Assess this cell for malaria.
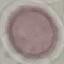

Uninfected.

Thin blood smear. Giemsa-stained preparation. Acquired by smartphone through the microscope eyepiece. Cell patch, automatically extracted from a larger field of view and resized to 64 × 64 pixels.